Evaluate for malaria.
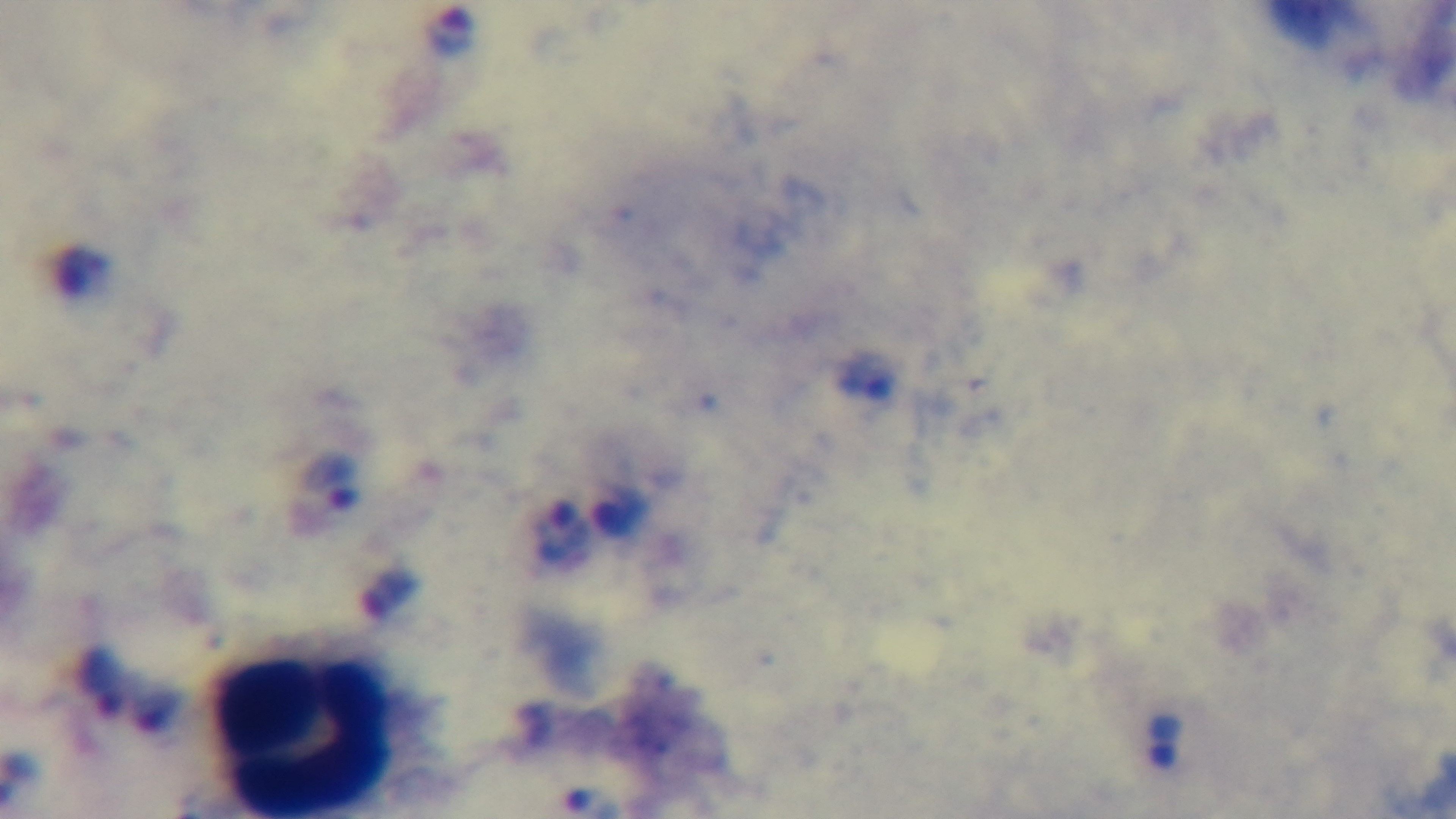
Positive.

Single field of view. Preparation: thick smear. Giemsa-stained. Mounted 4K digital camera. Light microscopy. 100x oil-immersion objective.